Report the malaria status of this cell.
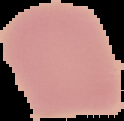
It is uninfected.

Summary:
  - Image size: 124×121 pixels
  - Preparation: thin blood smear
  - Image type: segmented cell region with the area outside set to black